Assess for Plasmodium parasites.
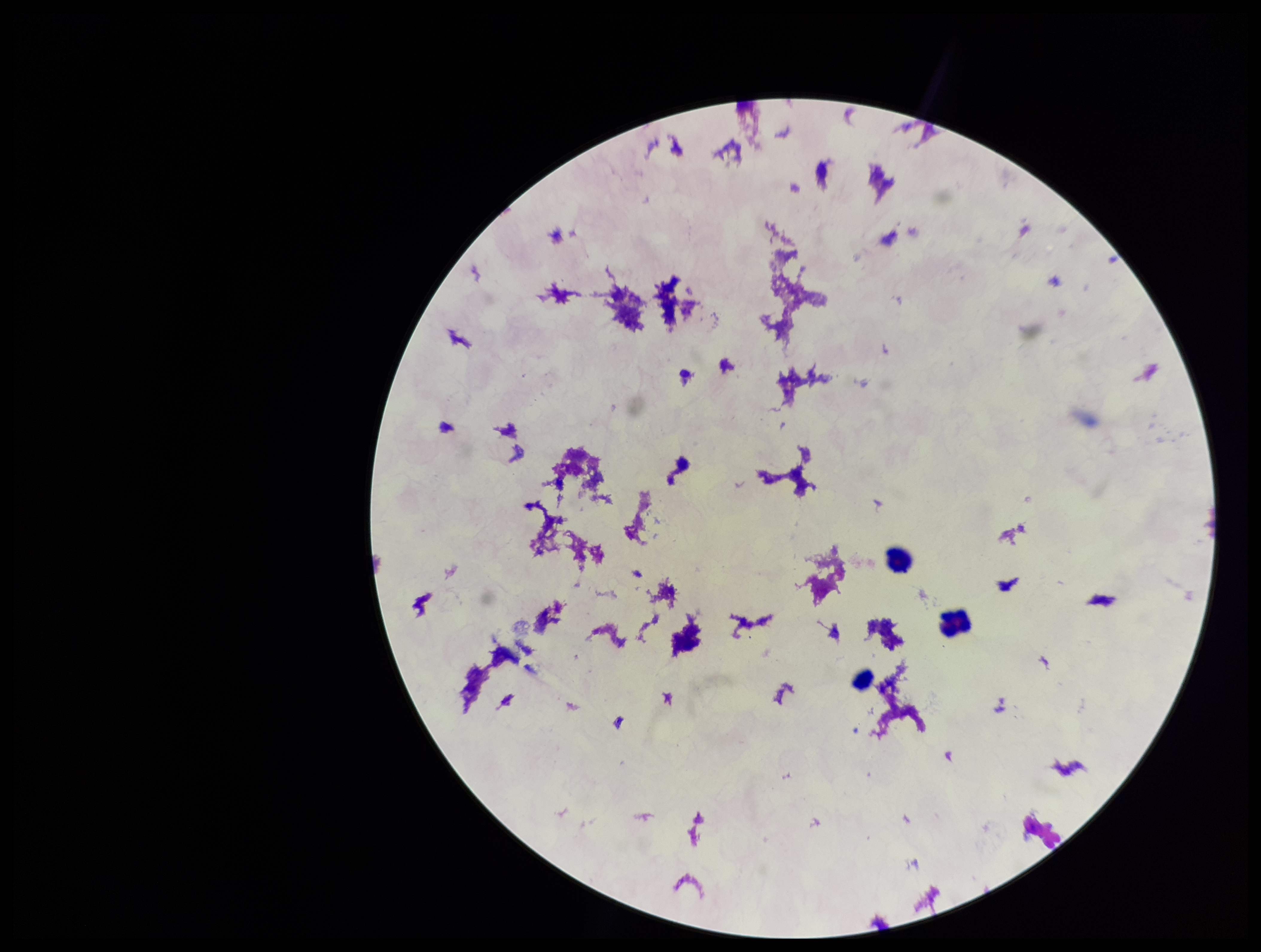
None seen.

preparation = thick smear
capture = smartphone photograph through the microscope eyepiece
parasite count = 0
stain = Giemsa
leukocyte count = 3
patient malaria status = negative
image size = 1261×952 pixels
field of view = single